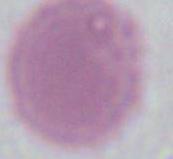
modality = micrograph
identification = red blood cell
magnification = 1000x